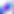

magnification: 400x
modality: photomicrograph
identification: Toxoplasma gondii